State which parasite is depicted.
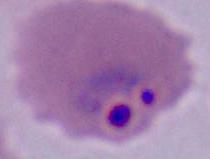
This is Plasmodium.

magnification = 400x or 1000x
modality = photomicrograph